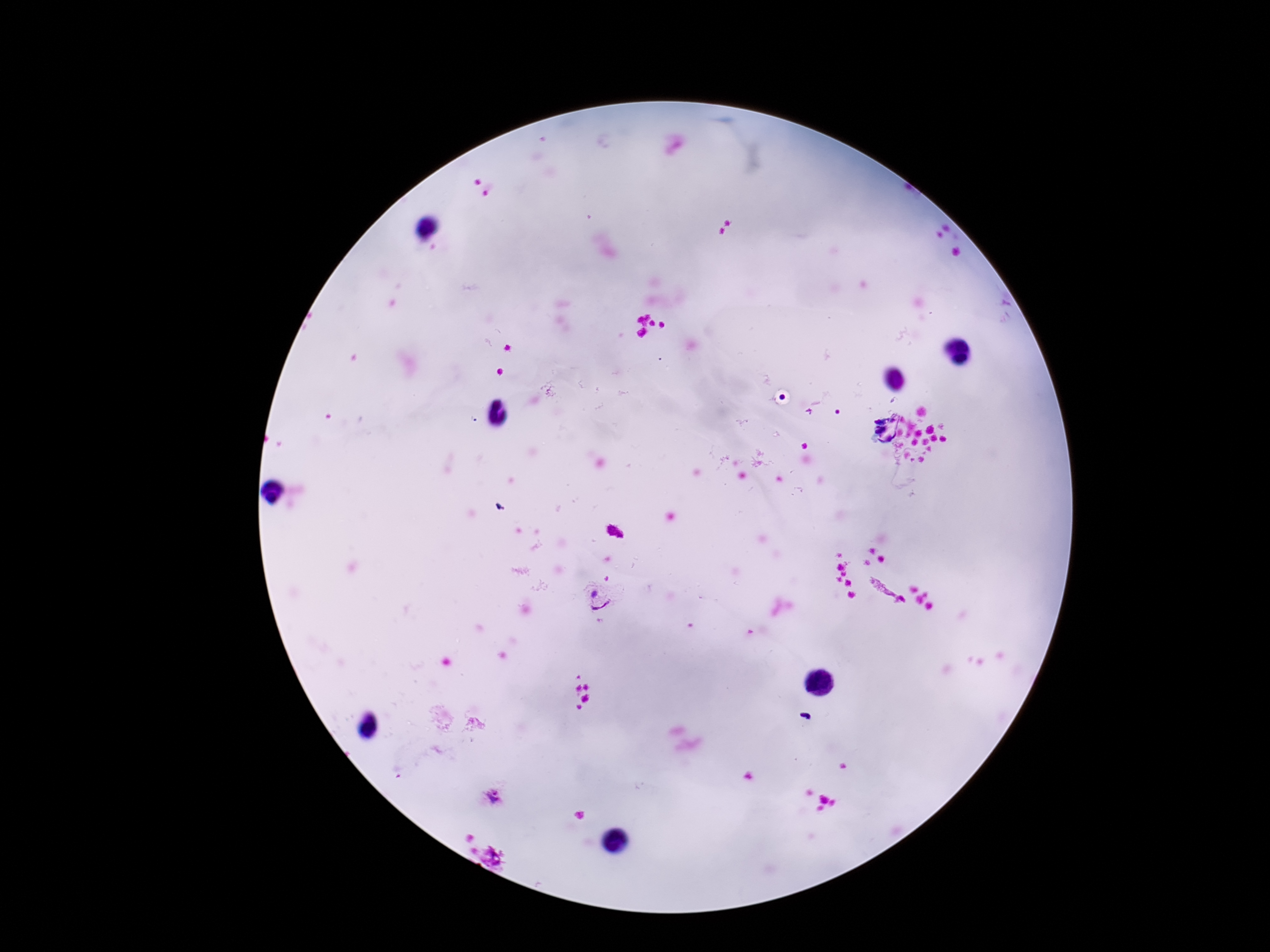

Approximate centers as (x, y) in pixels.
Summary:
  - Plasmodium parasite locations: (598, 600), (491, 797)
  - Preparation: thick peripheral-blood smear
  - Patient malaria status: infected
  - Image size: 1270×952 pixels
  - Capture: smartphone camera through the microscope eyepiece
  - Stain: Giemsa
  - Magnification: 100x
  - Field of view: single